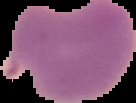

Summary:
  - Preparation: thin blood smear
  - Malaria status: parasitized
  - Image type: cell region segmented out of the field of view; surrounding area masked to black
  - Image size: 136×103 pixels